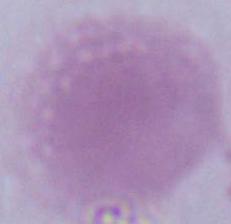

Summary:
  - Modality: micrograph
  - Magnification: 1000x
  - Identification: erythrocyte